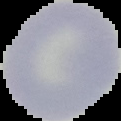

{
  "image_type": "segmented cell region with the area outside set to black",
  "result": "no malaria parasites seen",
  "preparation": "thin blood film",
  "image_size": "121×121 pixels"
}